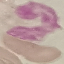

{
  "result": "no malaria parasites seen",
  "capture": "smartphone through the microscope eyepiece",
  "image_type": "cell patch, automatically extracted from a larger field of view and resized to 64 × 64 pixels",
  "stain": "Giemsa",
  "preparation": "thin blood smear"
}